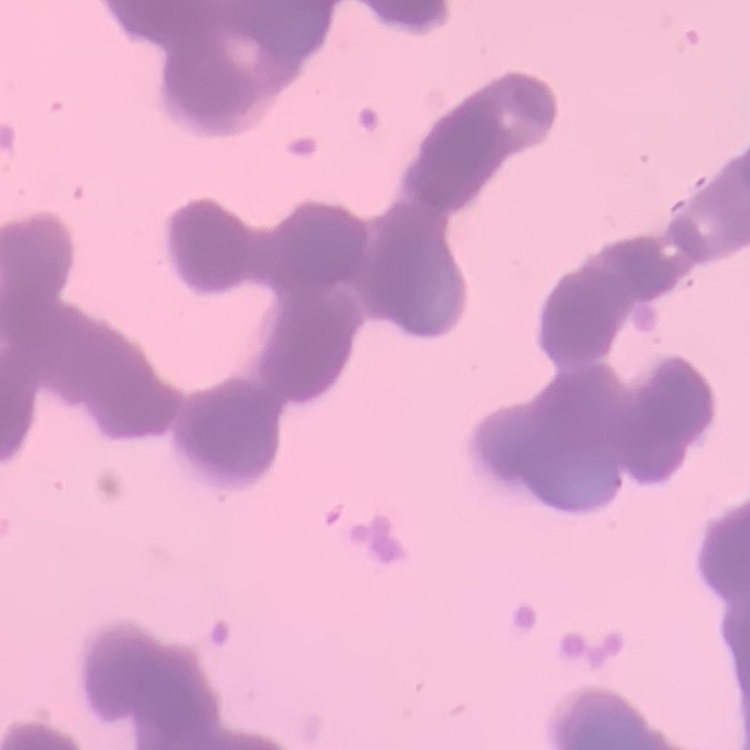
Summary:
  - Red blood cell morphology: rouleaux formation
  - Preparation: thin blood film
  - Image type: square crop of a larger photomicrograph
  - Stain: Field's or Giemsa